Describe the morphology of the red blood cells.
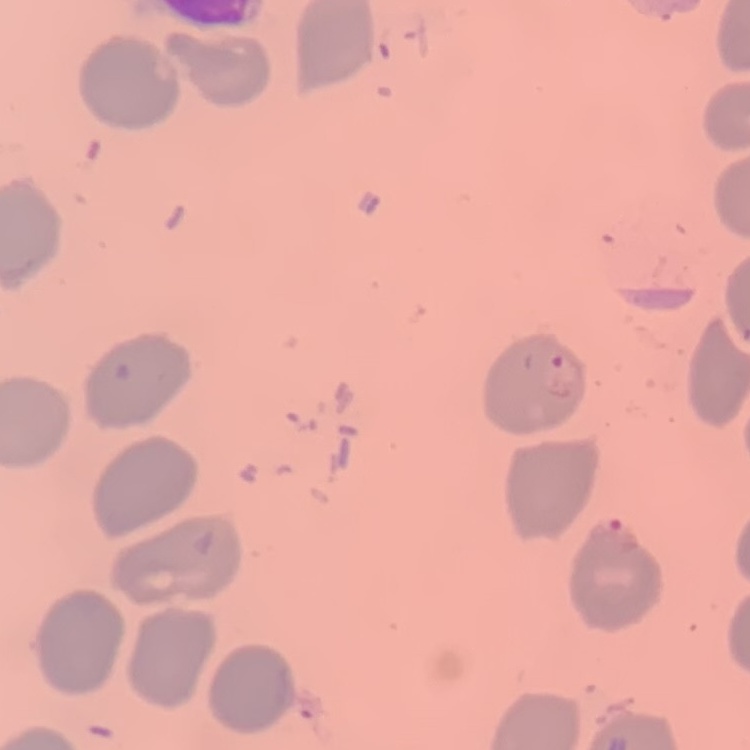
They show no rouleaux formation.

Summary:
  - Image type: one tile cut from a larger photomicrograph
  - Stain: Field's or Giemsa
  - Preparation: thin blood smear